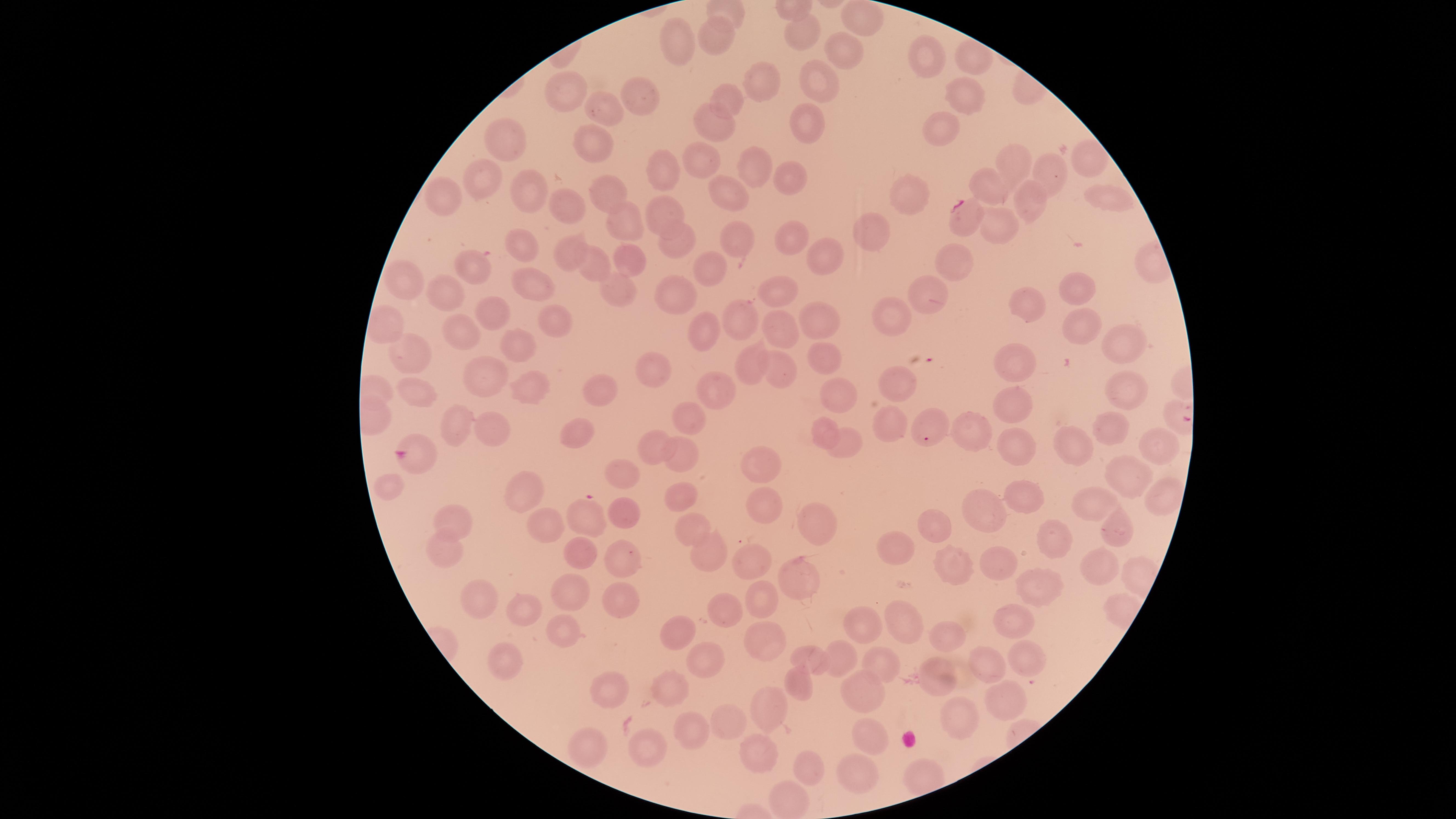

Approximate marker points as (x, y) in pixels. Uninfected red blood cells: (862, 21), (802, 28), (718, 40), (679, 45), (931, 52), (843, 55), (819, 81), (763, 82), (569, 93), (960, 94), (644, 96), (727, 101), (603, 111), (809, 115), (716, 126), (943, 126), (506, 145), (593, 152), (708, 159), (1013, 161), (1085, 161), (759, 164), (1050, 175), (659, 179), (484, 180), (790, 180), (989, 188), (727, 191), (909, 193), (1106, 193), (610, 194), (525, 196), (1029, 199), (443, 203), (565, 205), (663, 210), (625, 223), (995, 225), (877, 233), (791, 238), (678, 240), (730, 241), (522, 248), (815, 254), (570, 256), (628, 257), (954, 264), (599, 267), (712, 267), (474, 270), (407, 279), (532, 283), (616, 287), (1076, 289), (682, 291), (447, 295), (931, 295), (783, 296), (1033, 304), (488, 311), (897, 311), (821, 315), (733, 318), (548, 321), (1075, 323), (468, 328), (701, 331), (789, 331), (515, 343), (1126, 350), (825, 354), (408, 355), (749, 359), (1016, 362), (787, 368), (490, 370), (653, 370), (609, 383), (900, 383), (721, 385), (1129, 387), (533, 388), (838, 388), (417, 393), (1016, 408), (690, 414), (458, 424), (493, 427), (1113, 428), (822, 429), (972, 430), (578, 434), (1078, 439), (850, 441), (653, 445), (1155, 446), (1016, 450), (684, 456), (762, 465), (626, 471), (1123, 471), (391, 487), (1162, 493), (527, 494), (1026, 494), (683, 497), (761, 499), (1095, 503), (979, 509), (624, 513), (453, 518), (545, 523), (813, 525), (934, 525), (686, 529), (1119, 529), (1056, 538), (899, 542), (704, 548), (438, 551), (583, 555), (623, 557), (998, 562), (755, 564), (1096, 565), (952, 568), (799, 570), (569, 589), (1035, 591), (624, 594), (489, 602), (768, 604), (521, 612), (719, 613), (1011, 614), (859, 624), (913, 625), (563, 629), (680, 630), (948, 635), (763, 640), (1024, 655), (837, 656), (506, 657), (705, 660), (811, 660), (875, 664), (986, 666), (936, 676), (794, 682), (602, 689), (859, 689), (674, 691), (1005, 700), (768, 704), (957, 717), (720, 719), (692, 731), (867, 734), (589, 741), (650, 746), (755, 753), (807, 768), (858, 768). Parasitized red blood cells: (962, 217), (925, 439), (413, 455), (589, 512). Image is 1456×819 pixels. Species: Plasmodium falciparum. Presence: malaria parasites detected. Photographed with a smartphone camera through the microscope eyepiece. Giemsa stain. Circular visible region. Thin smear of blood. One field of view of the specimen.